Assess the morphology of the red blood cells.
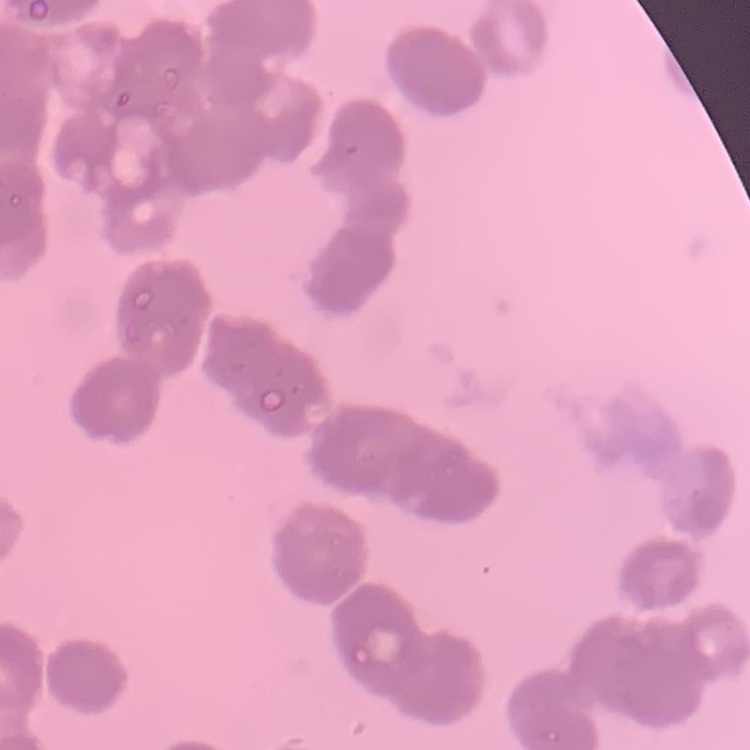

Rouleaux formation.

Field's or Giemsa stain. Thin peripheral smear. Square crop of a larger photomicrograph.